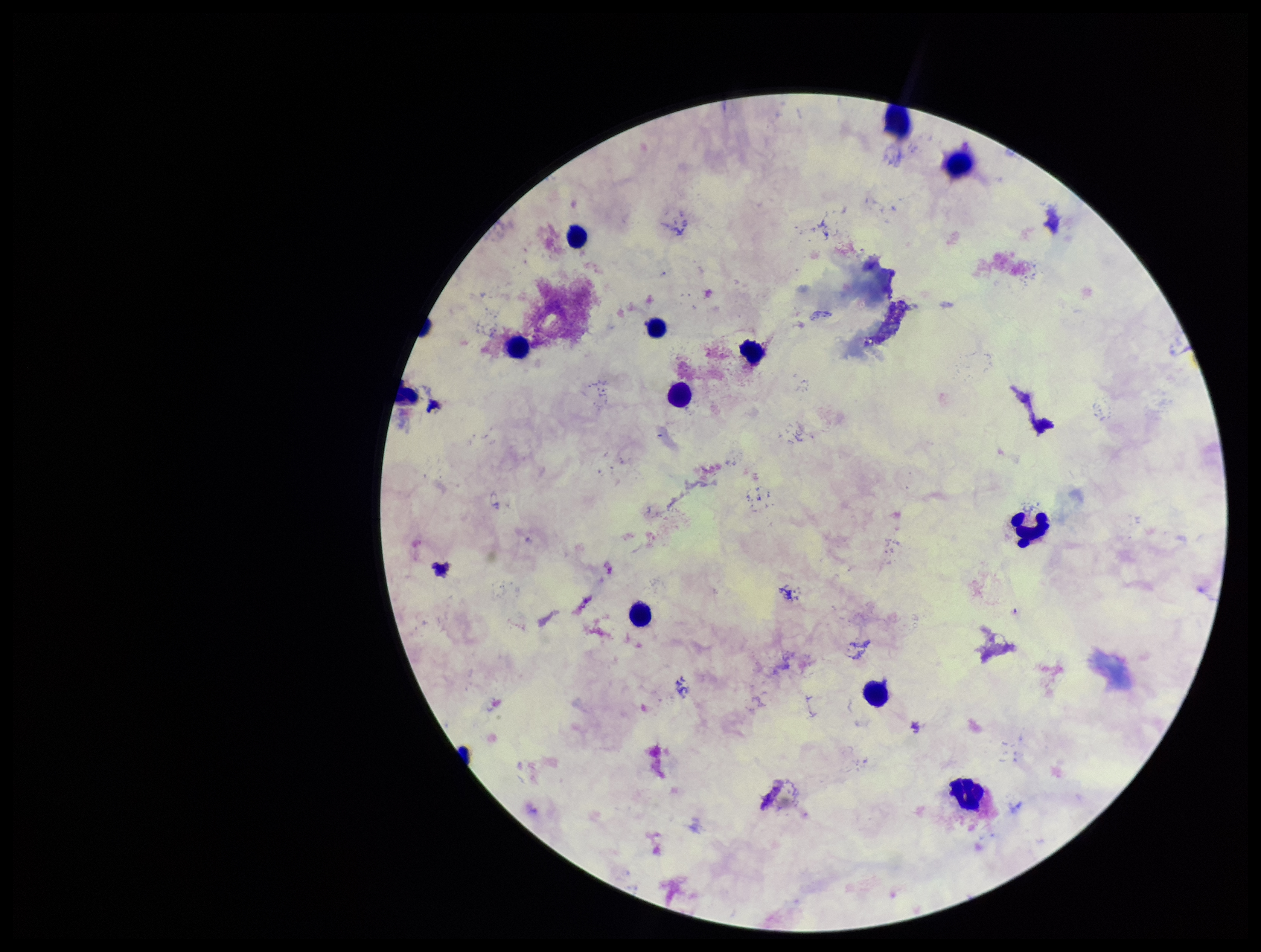
Giemsa stain. Plasmodium parasites: none seen. Preparation: thick. Patient malaria status: negative. Image is 1261×952 pixels. Photographed through the microscope eyepiece with a smartphone camera. Single field of view. Leukocyte count: 12. Parasite count: 0.